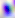
Toxoplasma gondii is shown. Captured at 400x magnification. Photomicrograph.